Identify the cell.
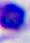
A leukocyte.

{
  "magnification": "400x",
  "modality": "photomicrograph"
}